Classify this cell by malaria status.
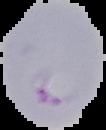
It is parasitized.

Image is 106×130 pixels. From a thin blood smear. Segmented cell region on a black background.